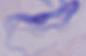
modality = micrograph
magnification = 1000x
identification = trypanosome